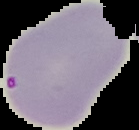

preparation = thin blood smear
image size = 139×130 pixels
image type = segmented cell region with the area outside set to black
malaria status = parasitized